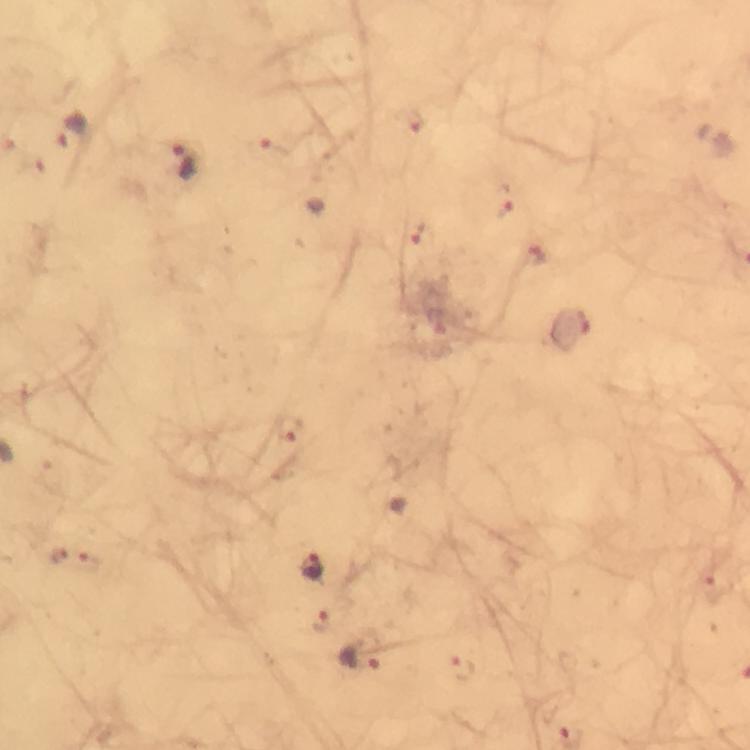

Approximate centers as [x, y] in pixels. Plasmodium parasite locations: [412, 121], [72, 132], [277, 146], [177, 164], [502, 203], [422, 237], [534, 255], [573, 333], [289, 427], [59, 555], [89, 565], [311, 566], [718, 585], [325, 621], [362, 662], [461, 669]. Immersion oil was used. 100x magnification. From a malaria diagnostic workup. Giemsa-stained preparation. Cropped region of a single field of view. Image is 750×750 pixels. Thick blood film. Photographed with a smartphone mounted on the microscope.